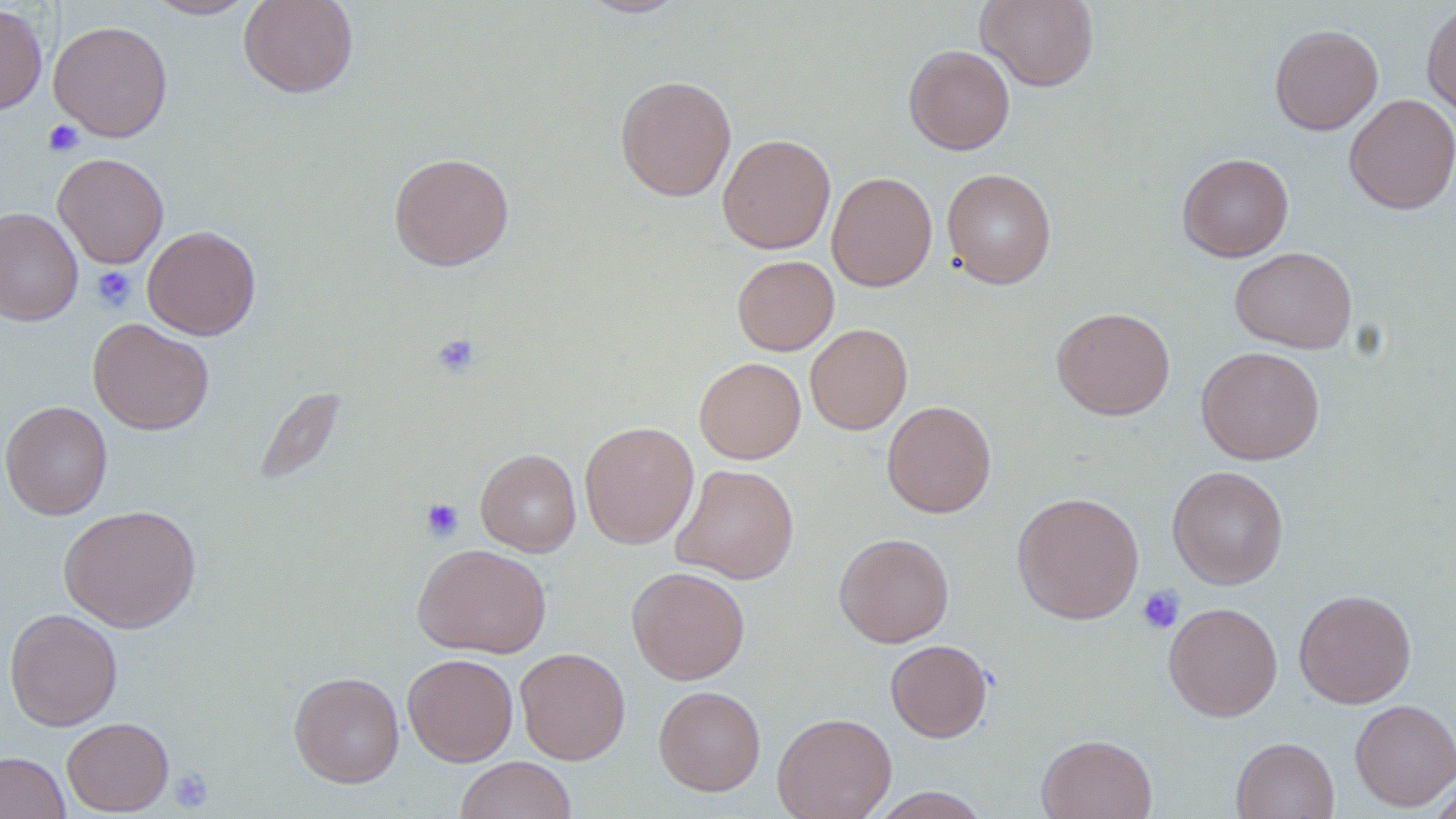

Approximate bounding boxes as (x1,y1)-(x2,y2) corner pairs in pixels. Platelet locations: (43,119)-(84,157), (90,265)-(136,312), (430,333)-(481,378), (420,497)-(464,543), (1136,586)-(1185,634), (169,768)-(214,813). Uninfected red blood cell locations: (145,0)-(258,19), (239,0)-(358,98), (579,0)-(688,18), (976,0)-(1099,91), (1421,2)-(1456,121), (0,4)-(47,115), (48,21)-(173,142), (1269,24)-(1383,135), (904,45)-(1015,154), (615,75)-(737,202), (1344,94)-(1456,214), (718,134)-(836,254), (52,152)-(169,268), (388,152)-(514,271), (1177,152)-(1294,261), (941,168)-(1057,289), (826,171)-(937,291), (0,207)-(83,326), (142,224)-(261,339), (1229,246)-(1357,354), (732,255)-(839,356), (1051,306)-(1175,420), (87,318)-(214,435), (805,323)-(913,435), (1196,345)-(1325,465), (694,357)-(806,464), (252,385)-(347,486), (0,400)-(113,520), (882,400)-(996,517), (579,421)-(699,549), (476,448)-(581,556), (671,463)-(799,584), (1167,466)-(1289,589), (1012,491)-(1144,624), (59,504)-(202,633), (834,533)-(954,648), (413,543)-(551,658), (626,566)-(750,685), (1293,589)-(1417,708), (1163,602)-(1283,722), (4,608)-(123,731), (885,639)-(992,742), (515,647)-(630,764), (402,652)-(518,766), (289,671)-(405,787), (653,685)-(766,795), (1349,698)-(1456,810), (772,712)-(897,819), (62,716)-(174,815), (1036,733)-(1157,819), (1231,736)-(1340,819), (0,751)-(70,819), (455,756)-(577,819), (1425,776)-(1456,819), (868,786)-(991,818). Slide-level diagnosis: negative for blood parasites. Image is 1456×819 pixels. Captured at 1000x magnification. Optical microscopy. Single field of view. Thin blood film. May-Grünwald-Giemsa stain.